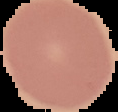

Summary:
  - Image size: 118×112 pixels
  - Preparation: thin blood smear
  - Result: no malaria parasites seen
  - Image type: cell region segmented out of the field of view; surrounding area masked to black